Assess this cell for malaria.
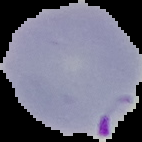
It is parasitized.

preparation = thin blood smear
image type = segmented cell region with the area outside set to black
image size = 142×142 pixels